Assess the morphology of the red blood cells.
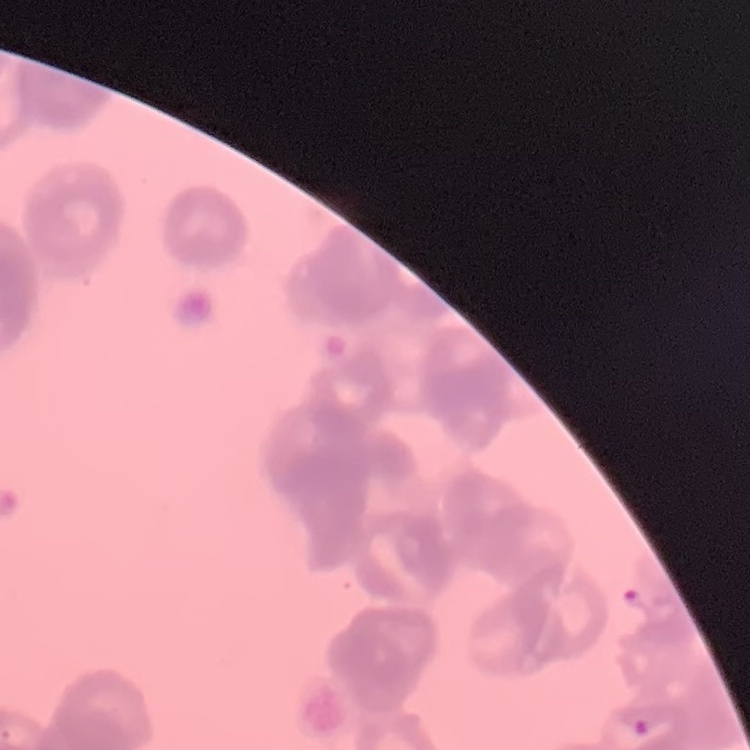
They show rouleaux formation.

Thin blood smear. One tile cut from a larger photomicrograph. Stained with either Field's or Giemsa.